Mark where platelets are.
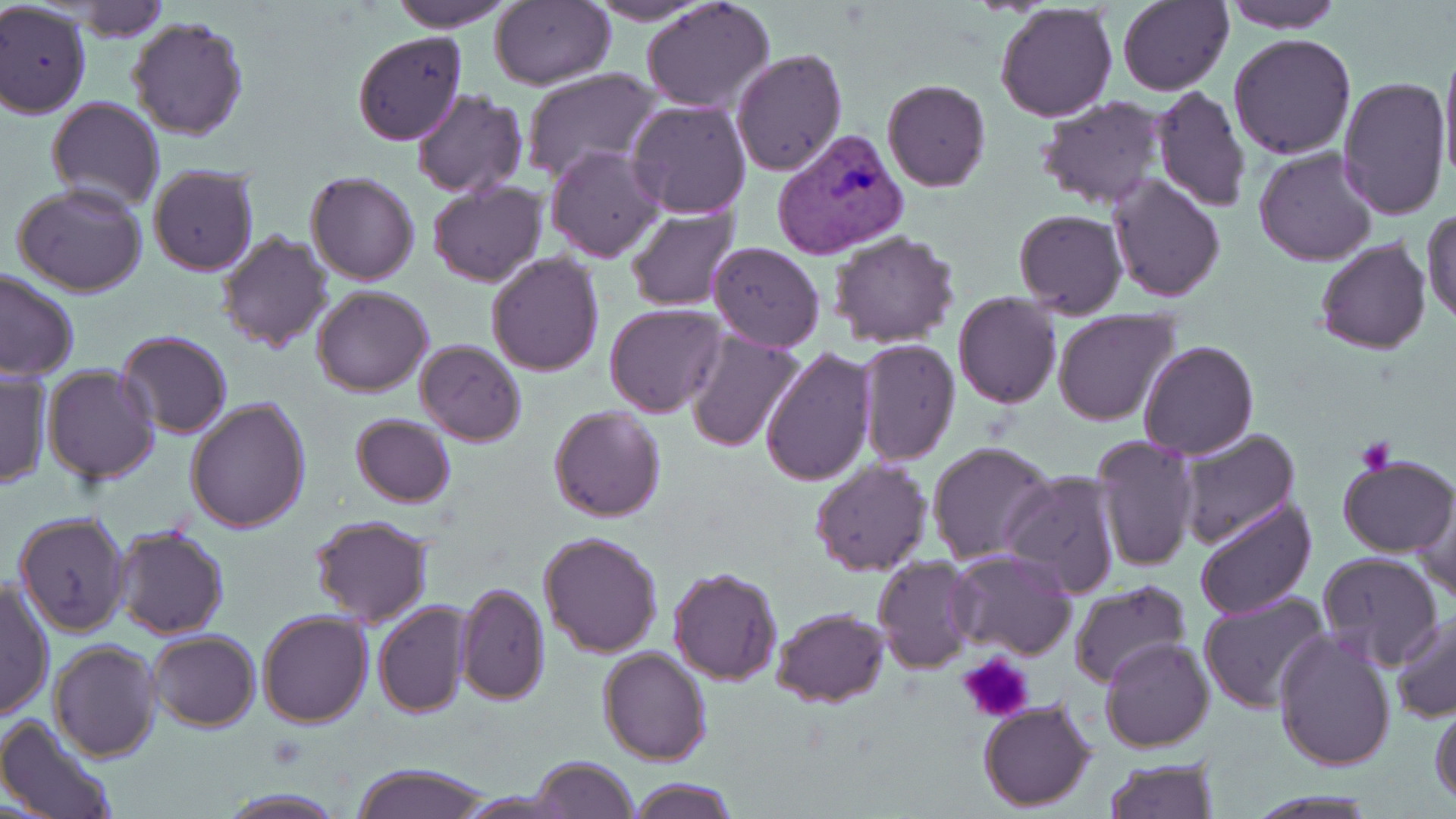

Approximate bounding boxes as (x1,y1)-(x2,y2) corner pairs in pixels.
Platelets: (1356,437)-(1395,475), (955,653)-(1034,724).

{
  "plasmodium_vivax_infected_red_blood_cell_locations": "approximate bounding boxes as (x1,y1)-(x2,y2) corner pairs in pixels: (771,128)-(911,260)",
  "slide_level_diagnosis": "Plasmodium vivax",
  "field_of_view": "single",
  "magnification": "1000x",
  "stain": "May-Grünwald-Giemsa",
  "uninfected_red_blood_cell_locations": "approximate bounding boxes as (x1,y1)-(x2,y2) corner pairs in pixels: (388,0)-(516,31), (492,0)-(616,89), (584,0)-(716,24), (642,0)-(775,115), (1117,0)-(1234,97), (1222,0)-(1344,34), (66,1)-(169,40), (994,3)-(1118,123), (0,4)-(91,119), (128,17)-(250,139), (351,31)-(468,146), (1229,32)-(1358,159), (1439,44)-(1456,190), (731,47)-(848,176), (519,67)-(661,185), (1337,74)-(1451,219), (881,78)-(991,192), (1150,83)-(1251,213), (410,89)-(527,199), (44,96)-(164,212), (1035,96)-(1167,209), (625,100)-(751,220), (546,145)-(665,263), (1254,148)-(1378,265), (148,166)-(260,277), (304,171)-(422,286), (1108,173)-(1226,302), (427,180)-(546,288), (11,183)-(149,297), (624,203)-(742,311), (1013,209)-(1128,318), (1424,210)-(1456,329), (215,228)-(334,352), (828,231)-(960,349), (1315,238)-(1432,356), (707,241)-(825,352), (485,251)-(604,376), (0,270)-(79,382), (312,286)-(433,397), (952,292)-(1063,409), (604,304)-(727,418), (1051,309)-(1180,427), (116,329)-(233,438), (685,329)-(805,453), (855,337)-(958,468), (415,340)-(526,446), (1137,340)-(1258,460), (760,347)-(876,488), (42,364)-(160,484), (0,368)-(52,489), (185,396)-(312,535), (549,405)-(667,522), (351,413)-(457,508), (1175,427)-(1303,551), (1090,434)-(1201,572), (927,441)-(1058,566), (1336,454)-(1454,557), (810,457)-(932,576), (999,468)-(1124,600), (1413,493)-(1455,605), (1192,497)-(1320,622), (13,511)-(132,637), (307,513)-(434,626), (113,525)-(230,640), (539,530)-(663,657), (948,549)-(1078,659), (1316,551)-(1444,671), (872,556)-(977,672), (666,566)-(783,684), (0,578)-(54,722), (1068,578)-(1192,692), (455,581)-(550,704), (1197,590)-(1331,714), (373,601)-(471,719), (770,606)-(889,708), (257,610)-(373,729), (1390,612)-(1456,723), (1272,629)-(1397,772), (148,630)-(260,732), (1100,636)-(1215,753), (48,639)-(162,762), (598,646)-(711,765), (977,698)-(1098,813), (1429,702)-(1456,807), (0,712)-(119,819), (531,756)-(639,818), (1103,757)-(1219,818), (348,763)-(493,819), (628,777)-(738,819), (217,788)-(348,818)",
  "modality": "optical microscopy",
  "preparation": "thin blood smear",
  "image_size": "1456×819 pixels"
}